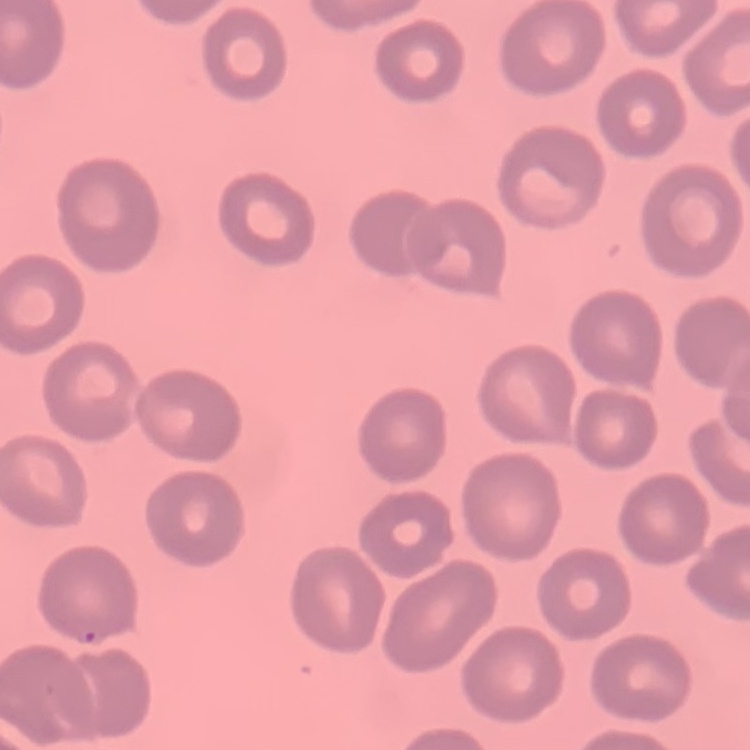
Summary:
  - Erythrocyte morphology: no rouleaux formation
  - Preparation: thin peripheral smear
  - Stain: Field's or Giemsa
  - Image type: square crop of a larger photomicrograph